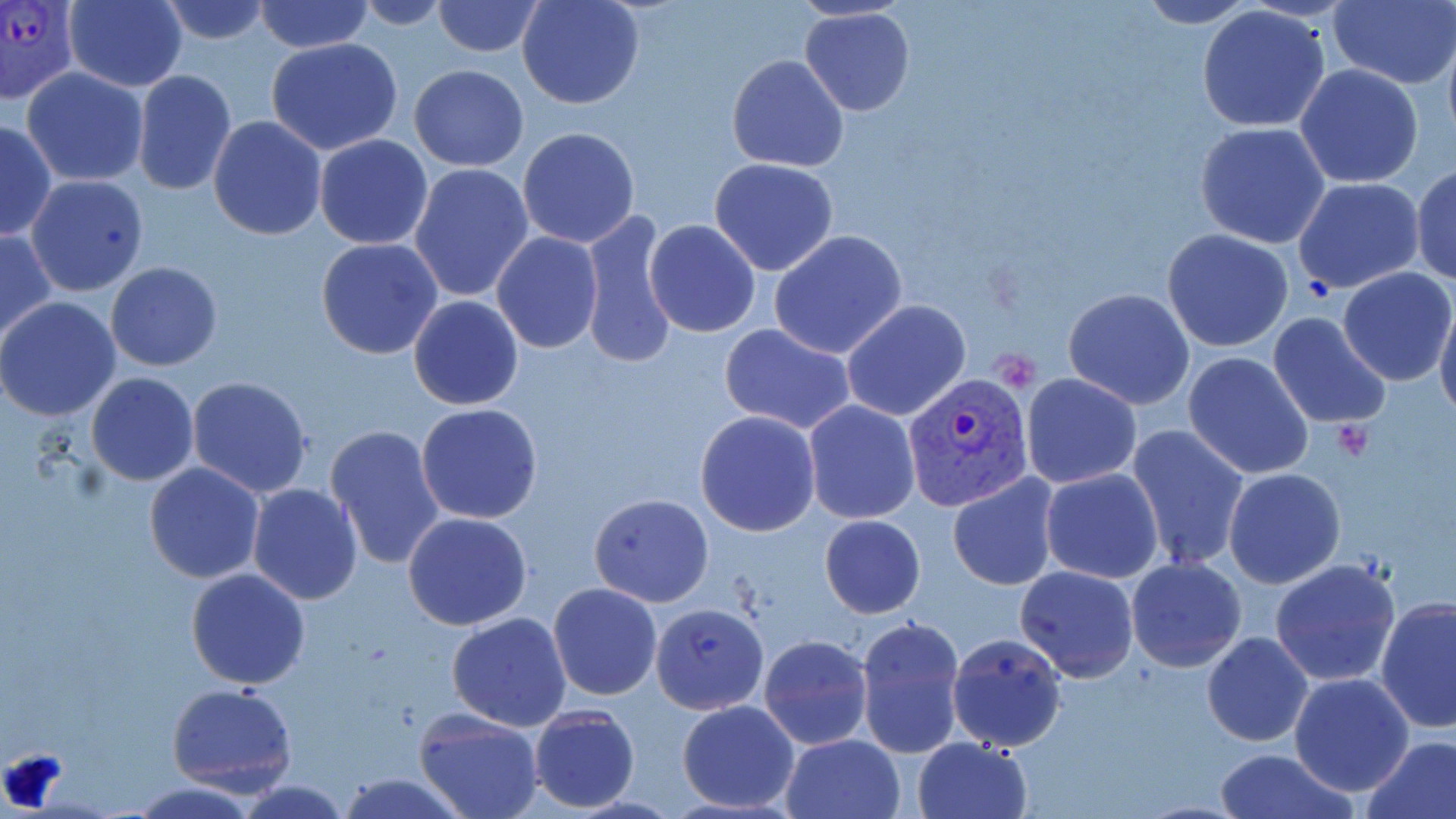

Summary:
  - Coordinate format: approximate bounding boxes as named x1/y1/x2/y2 corners in pixels
  - Plasmodium vivax-infected red blood cell locations: (x1=0, y1=0, x2=83, y2=105), (x1=903, y1=374, x2=1034, y2=511)
  - Uninfected red blood cell locations: (x1=156, y1=0, x2=275, y2=45), (x1=252, y1=0, x2=376, y2=53), (x1=432, y1=0, x2=545, y2=57), (x1=517, y1=0, x2=644, y2=110), (x1=1130, y1=0, x2=1263, y2=28), (x1=62, y1=1, x2=188, y2=90), (x1=348, y1=1, x2=459, y2=29), (x1=1327, y1=1, x2=1456, y2=90), (x1=1194, y1=6, x2=1333, y2=133), (x1=800, y1=8, x2=916, y2=117), (x1=1442, y1=34, x2=1456, y2=153), (x1=266, y1=37, x2=405, y2=154), (x1=726, y1=55, x2=848, y2=173), (x1=1295, y1=64, x2=1425, y2=188), (x1=408, y1=65, x2=529, y2=170), (x1=21, y1=67, x2=148, y2=186), (x1=132, y1=70, x2=236, y2=196), (x1=208, y1=116, x2=326, y2=240), (x1=1, y1=120, x2=55, y2=242), (x1=1194, y1=122, x2=1331, y2=248), (x1=516, y1=127, x2=640, y2=249), (x1=314, y1=134, x2=433, y2=251), (x1=709, y1=157, x2=840, y2=276), (x1=1411, y1=161, x2=1456, y2=287), (x1=408, y1=163, x2=534, y2=304), (x1=26, y1=174, x2=148, y2=296), (x1=1293, y1=178, x2=1424, y2=294), (x1=580, y1=210, x2=679, y2=371), (x1=644, y1=220, x2=761, y2=337), (x1=1, y1=229, x2=55, y2=345), (x1=1162, y1=229, x2=1294, y2=352), (x1=769, y1=230, x2=910, y2=360), (x1=491, y1=232, x2=603, y2=354), (x1=316, y1=238, x2=443, y2=358), (x1=106, y1=260, x2=223, y2=372), (x1=1339, y1=266, x2=1455, y2=384), (x1=1063, y1=288, x2=1196, y2=411), (x1=408, y1=295, x2=524, y2=410), (x1=0, y1=297, x2=121, y2=422), (x1=1436, y1=297, x2=1456, y2=425), (x1=842, y1=300, x2=970, y2=421), (x1=1266, y1=313, x2=1392, y2=429), (x1=718, y1=323, x2=857, y2=434), (x1=1182, y1=349, x2=1314, y2=479), (x1=85, y1=373, x2=199, y2=487), (x1=1022, y1=374, x2=1143, y2=489), (x1=186, y1=377, x2=313, y2=498), (x1=804, y1=401, x2=921, y2=522), (x1=415, y1=403, x2=544, y2=526), (x1=694, y1=410, x2=820, y2=537), (x1=324, y1=423, x2=446, y2=569), (x1=1126, y1=425, x2=1249, y2=573), (x1=143, y1=462, x2=265, y2=585), (x1=1223, y1=467, x2=1345, y2=589), (x1=1040, y1=468, x2=1164, y2=584), (x1=947, y1=474, x2=1061, y2=591), (x1=246, y1=483, x2=362, y2=605), (x1=1030, y1=492, x2=1165, y2=657), (x1=588, y1=494, x2=713, y2=607), (x1=403, y1=512, x2=533, y2=630), (x1=820, y1=514, x2=926, y2=618), (x1=573, y1=524, x2=693, y2=689), (x1=1126, y1=557, x2=1249, y2=673), (x1=1269, y1=558, x2=1400, y2=687), (x1=1014, y1=565, x2=1139, y2=683), (x1=186, y1=567, x2=311, y2=690), (x1=549, y1=584, x2=662, y2=700), (x1=1376, y1=595, x2=1456, y2=735), (x1=651, y1=602, x2=769, y2=714), (x1=446, y1=613, x2=572, y2=731), (x1=855, y1=614, x2=967, y2=758), (x1=946, y1=632, x2=1068, y2=752), (x1=1202, y1=632, x2=1314, y2=746), (x1=758, y1=635, x2=872, y2=751), (x1=1289, y1=671, x2=1416, y2=796), (x1=166, y1=682, x2=297, y2=794), (x1=677, y1=700, x2=800, y2=814), (x1=527, y1=706, x2=640, y2=812), (x1=413, y1=708, x2=545, y2=819), (x1=781, y1=733, x2=906, y2=819), (x1=1361, y1=735, x2=1456, y2=819), (x1=914, y1=737, x2=1032, y2=819), (x1=1214, y1=748, x2=1355, y2=819), (x1=335, y1=771, x2=471, y2=819), (x1=129, y1=779, x2=262, y2=818), (x1=231, y1=779, x2=354, y2=818)
  - Slide-level diagnosis: Plasmodium vivax
  - Image size: 1456×819 pixels
  - Modality: optical microscopy
  - Stain: May-Grünwald-Giemsa
  - Preparation: thin blood smear
  - Field of view: one of a larger specimen
  - Magnification: 1000x